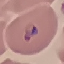 Result: malaria parasites detected. Acquired by smartphone through the microscope eyepiece. Cell patch, automatically extracted from a larger field of view and resized to 64 × 64 pixels. Giemsa stain. Thin blood film.